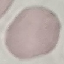
Summary:
  - Malaria status: uninfected
  - Stain: Giemsa
  - Image type: cell patch, automatically extracted from a larger field of view and resized to 64 × 64 pixels
  - Preparation: thin blood film
  - Capture: smartphone camera at the microscope eyepiece